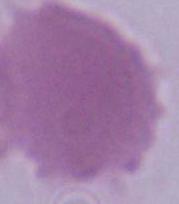

magnification = 1000x
modality = photomicrograph
identification = erythrocyte